Point out each Plasmodium parasite.
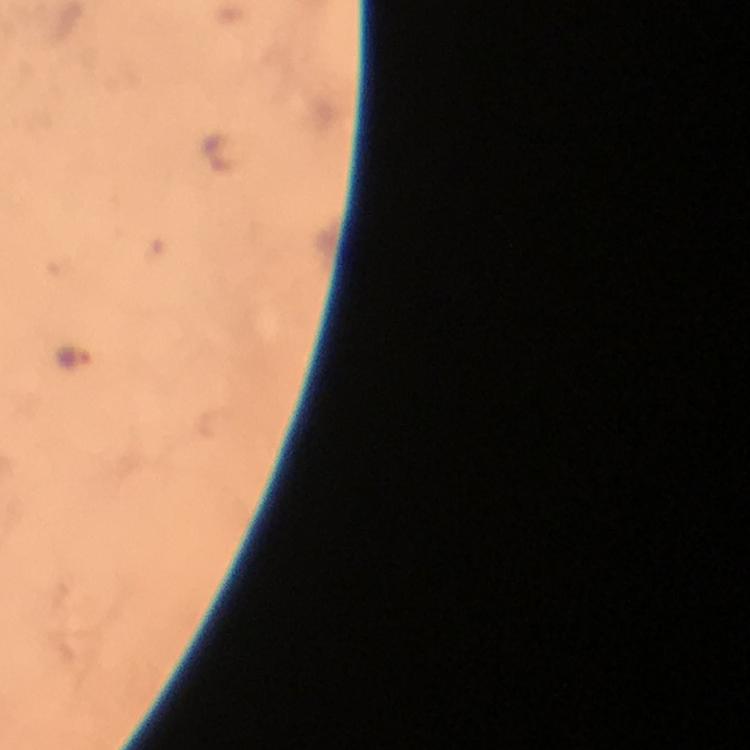

Approximate centers as [x, y] in pixels.
Plasmodium parasites: [76, 356].

capture = smartphone photograph through a microscope
cropped from = one field of view
immersion oil = used
preparation = thick blood smear
image size = 750×750 pixels
context = from a diagnostic examination for malaria
stain = Giemsa
magnification = 100x